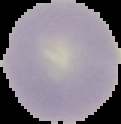

image type = segmented cell region with the area outside set to black
image size = 121×124 pixels
malaria status = uninfected
preparation = thin blood film